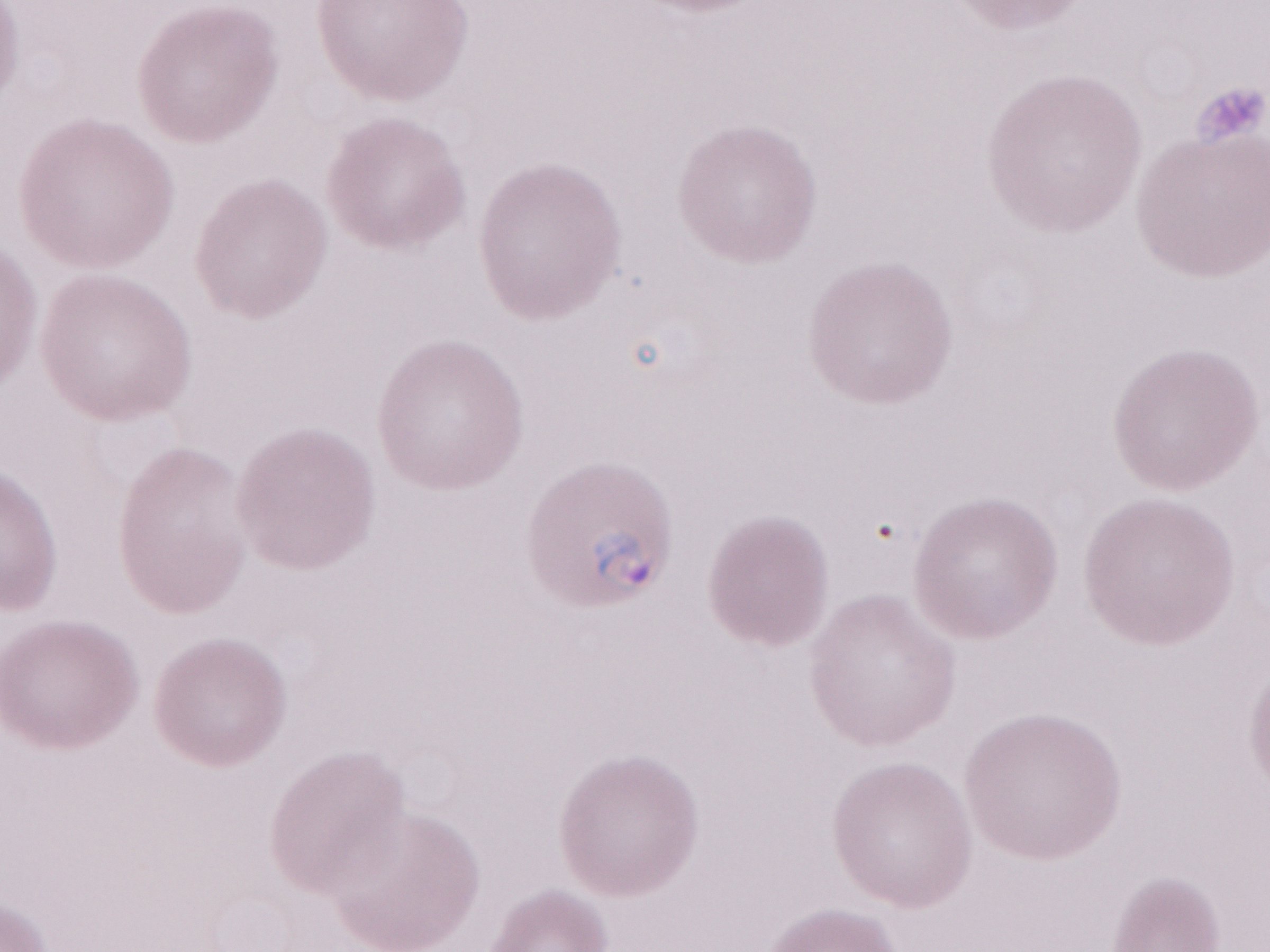 Magnification: 1,000x. Thin blood film. Single field of view. Image is 1270×952 pixels. Malaria diagnosis (patient-level): positive. Olympus BX43 microscope, Olympus DP73 camera. May-Grünwald-Giemsa (MGG) stain.